Comment on the morphology of the red blood cells.
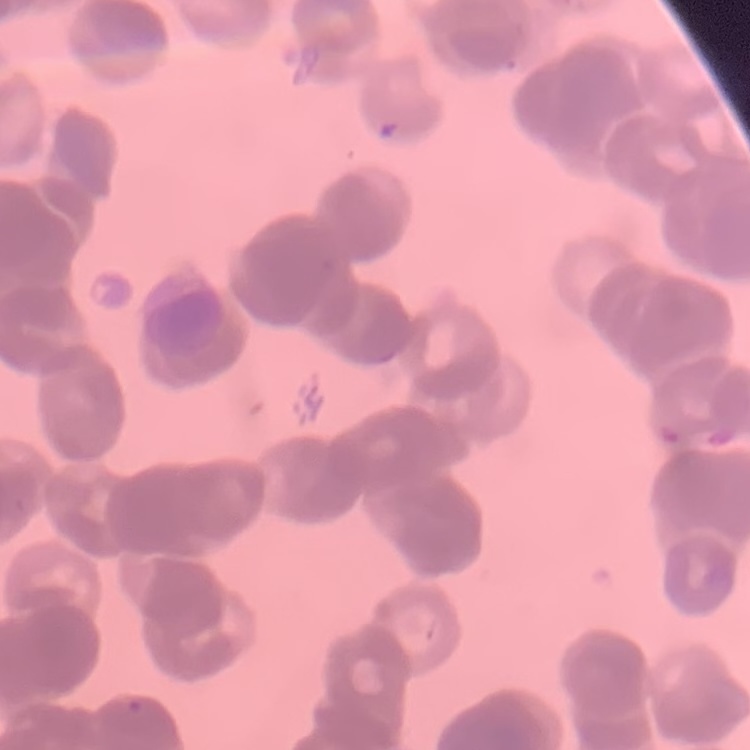

Rouleaux formation.

Summary:
  - Image type: one tile cut from a larger photomicrograph
  - Stain: Field's or Giemsa
  - Preparation: thin blood smear